Give the extent of all Plasmodium falciparum-infected red blood cells.
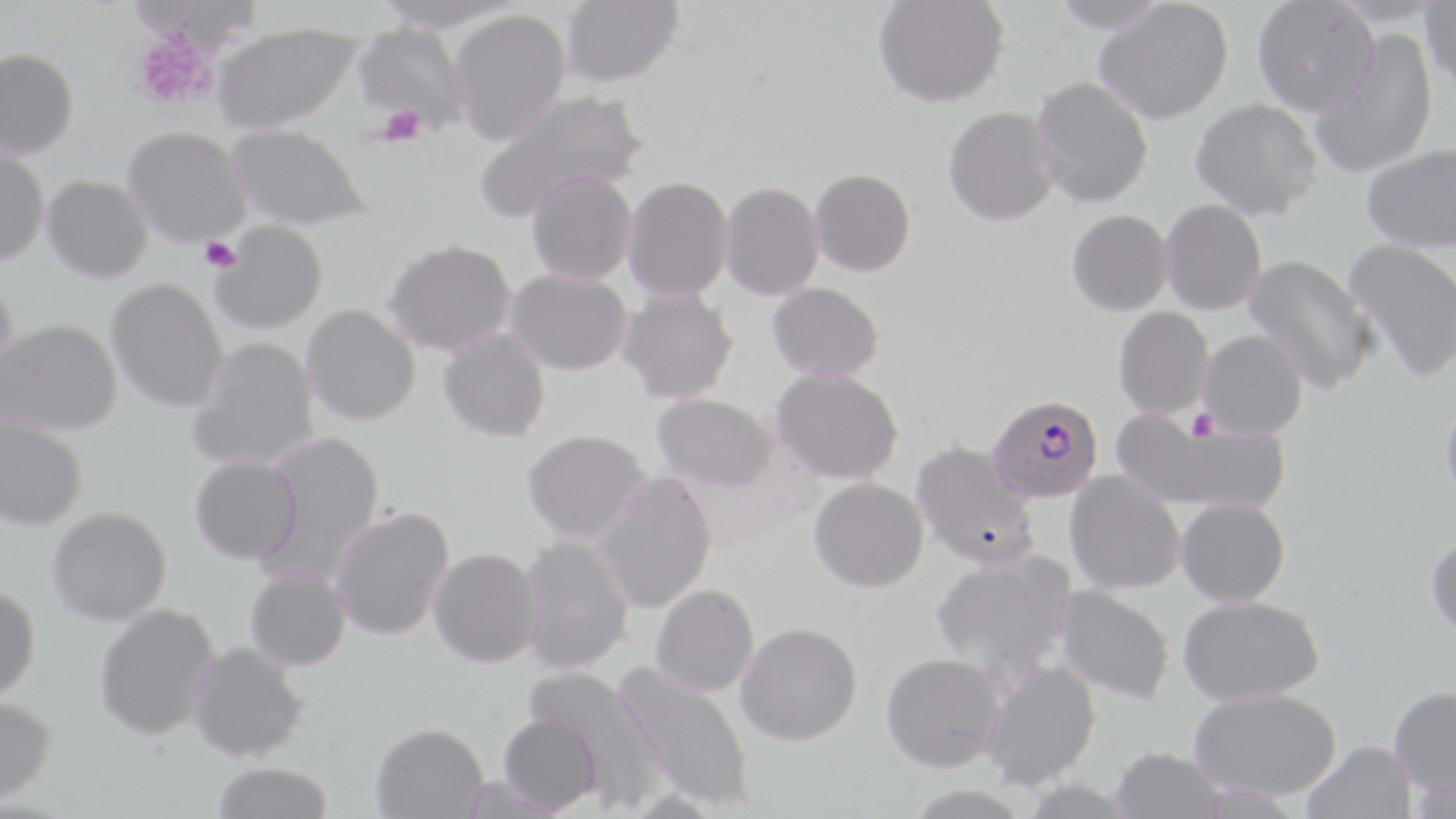
Approximate bounding boxes as named x1/y1/x2/y2 corners in pixels.
Plasmodium falciparum-infected red blood cells: (x1=986, y1=394, x2=1104, y2=504).

{
  "slide_level_diagnosis": "Plasmodium falciparum",
  "uninfected_red_blood_cell_locations": "approximate bounding boxes as named x1/y1/x2/y2 corners in pixels: (x1=561, y1=0, x2=684, y2=90), (x1=873, y1=0, x2=1009, y2=109), (x1=1049, y1=0, x2=1171, y2=33), (x1=1094, y1=1, x2=1233, y2=125), (x1=1252, y1=1, x2=1379, y2=117), (x1=1419, y1=2, x2=1456, y2=93), (x1=449, y1=10, x2=571, y2=147), (x1=351, y1=23, x2=471, y2=134), (x1=213, y1=24, x2=363, y2=135), (x1=1309, y1=29, x2=1438, y2=180), (x1=0, y1=49, x2=78, y2=162), (x1=1031, y1=76, x2=1153, y2=209), (x1=474, y1=88, x2=648, y2=224), (x1=1191, y1=98, x2=1323, y2=221), (x1=943, y1=106, x2=1061, y2=227), (x1=225, y1=125, x2=370, y2=232), (x1=122, y1=129, x2=253, y2=249), (x1=1361, y1=143, x2=1456, y2=253), (x1=0, y1=147, x2=49, y2=268), (x1=810, y1=168, x2=916, y2=277), (x1=526, y1=171, x2=637, y2=285), (x1=42, y1=176, x2=153, y2=284), (x1=622, y1=176, x2=733, y2=303), (x1=720, y1=181, x2=825, y2=301), (x1=1160, y1=200, x2=1267, y2=316), (x1=1067, y1=210, x2=1173, y2=316), (x1=209, y1=221, x2=328, y2=335), (x1=1343, y1=238, x2=1456, y2=383), (x1=384, y1=240, x2=516, y2=357), (x1=1243, y1=253, x2=1377, y2=395), (x1=505, y1=269, x2=632, y2=376), (x1=0, y1=277, x2=18, y2=386), (x1=105, y1=279, x2=228, y2=412), (x1=767, y1=282, x2=884, y2=382), (x1=617, y1=289, x2=739, y2=405), (x1=301, y1=304, x2=421, y2=426), (x1=1113, y1=307, x2=1214, y2=420), (x1=1, y1=321, x2=122, y2=437), (x1=437, y1=327, x2=551, y2=444), (x1=1198, y1=329, x2=1308, y2=440), (x1=188, y1=338, x2=321, y2=471), (x1=771, y1=367, x2=904, y2=485), (x1=1439, y1=390, x2=1456, y2=509), (x1=651, y1=392, x2=779, y2=493), (x1=1113, y1=410, x2=1290, y2=515), (x1=0, y1=412, x2=88, y2=532), (x1=522, y1=429, x2=652, y2=545), (x1=256, y1=431, x2=386, y2=583), (x1=910, y1=440, x2=1039, y2=571), (x1=189, y1=454, x2=302, y2=565), (x1=1064, y1=471, x2=1185, y2=595), (x1=591, y1=472, x2=717, y2=614), (x1=809, y1=477, x2=929, y2=593), (x1=1176, y1=497, x2=1290, y2=608), (x1=329, y1=505, x2=455, y2=641), (x1=46, y1=506, x2=172, y2=626), (x1=1425, y1=532, x2=1456, y2=641), (x1=519, y1=533, x2=635, y2=674), (x1=428, y1=548, x2=543, y2=667), (x1=931, y1=549, x2=1078, y2=687), (x1=245, y1=568, x2=352, y2=671), (x1=650, y1=583, x2=760, y2=697), (x1=1054, y1=585, x2=1175, y2=705), (x1=0, y1=586, x2=41, y2=703), (x1=1178, y1=595, x2=1324, y2=706), (x1=93, y1=603, x2=220, y2=740), (x1=736, y1=622, x2=862, y2=745), (x1=188, y1=642, x2=309, y2=762), (x1=881, y1=652, x2=1005, y2=772), (x1=980, y1=657, x2=1102, y2=792), (x1=615, y1=663, x2=755, y2=811), (x1=523, y1=665, x2=666, y2=809), (x1=1388, y1=686, x2=1456, y2=795), (x1=1189, y1=688, x2=1342, y2=802), (x1=0, y1=696, x2=57, y2=804), (x1=498, y1=713, x2=602, y2=815), (x1=370, y1=722, x2=489, y2=818), (x1=1301, y1=741, x2=1417, y2=819), (x1=1109, y1=746, x2=1227, y2=819), (x1=210, y1=762, x2=333, y2=819)",
  "magnification": "1000x",
  "field_of_view": "single",
  "preparation": "thin blood film",
  "stain": "May-Grünwald-Giemsa",
  "modality": "optical microscopy",
  "platelet_locations": "approximate bounding boxes as named x1/y1/x2/y2 corners in pixels: (x1=131, y1=30, x2=219, y2=112), (x1=378, y1=105, x2=426, y2=147), (x1=198, y1=236, x2=242, y2=273), (x1=1187, y1=409, x2=1220, y2=441)",
  "image_size": "1456×819 pixels"
}